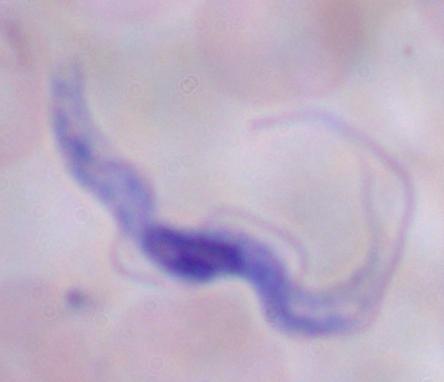 1000x magnification. A trypanosome is seen. Micrograph.